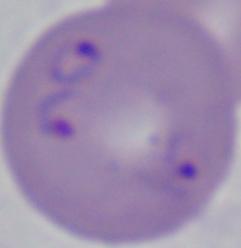
{
  "identification": "Babesia",
  "modality": "photomicrograph",
  "magnification": "1000x"
}